Point out each malaria parasite and each leukocyte.
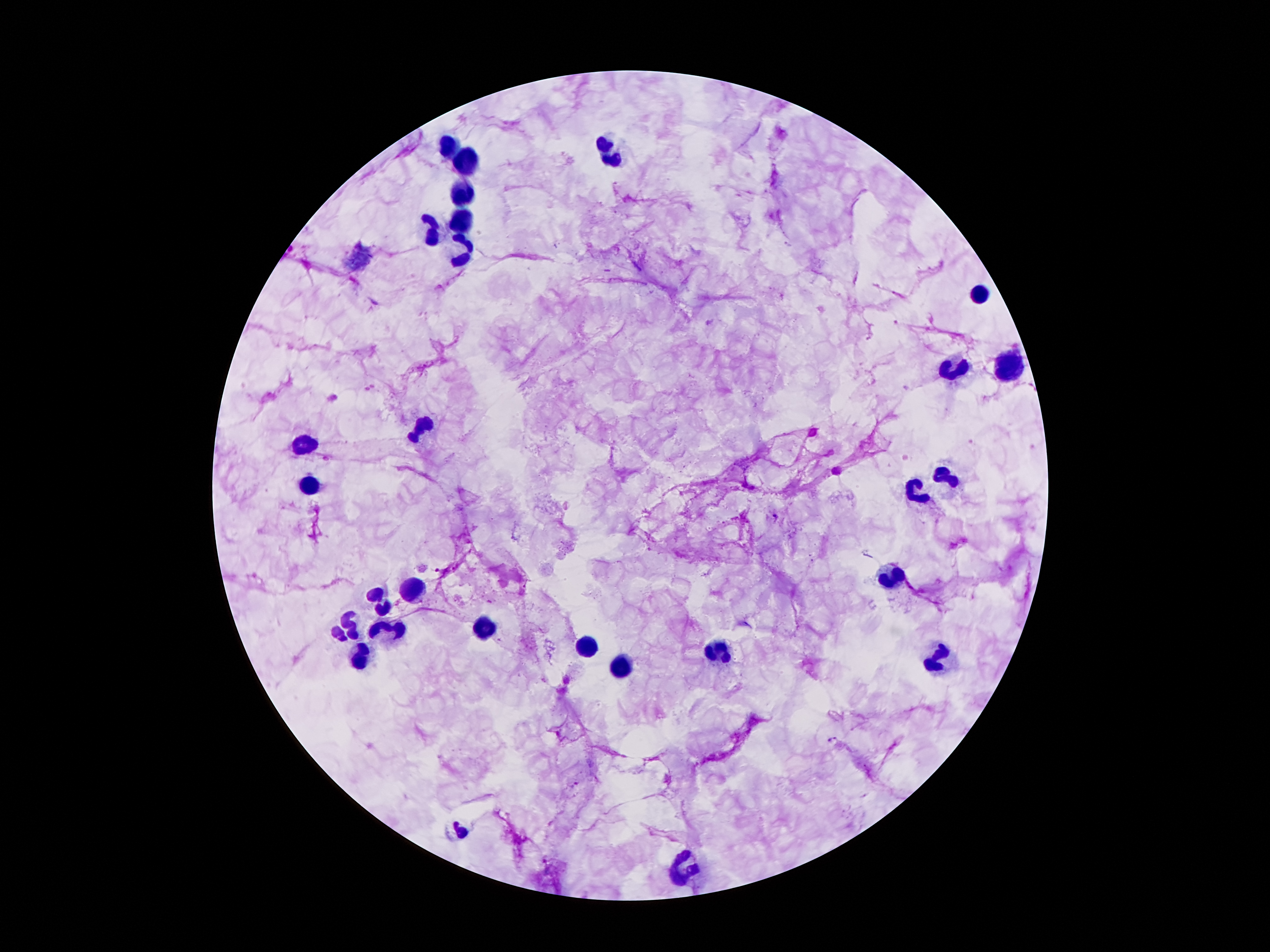

Approximate centers as (x, y) in pixels.
Malaria parasites: (775, 518), (834, 739).
Leukocytes: (449, 143), (610, 158), (464, 162), (466, 196), (468, 220), (436, 229), (468, 251), (979, 294), (1010, 363), (953, 370), (424, 426), (301, 445), (948, 474), (309, 488), (917, 496), (893, 576), (418, 588), (382, 604), (351, 627), (488, 629), (385, 632), (590, 645), (720, 651), (360, 659), (937, 662), (623, 666), (683, 869).

Giemsa stain. Patient malaria status: infected with Plasmodium falciparum. Thick blood smear. Image is 1270×952 pixels. Smartphone photograph taken through the microscope eyepiece. Single field of view. 100x magnification.